Classify this cell by malaria status.
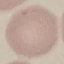

Uninfected.

Summary:
  - Image type: automatically extracted cell patch, resized to 64 × 64 pixels
  - Preparation: thin blood smear
  - Stain: Giemsa
  - Capture: smartphone through the microscope eyepiece